Comment on the morphology of the red blood cells.
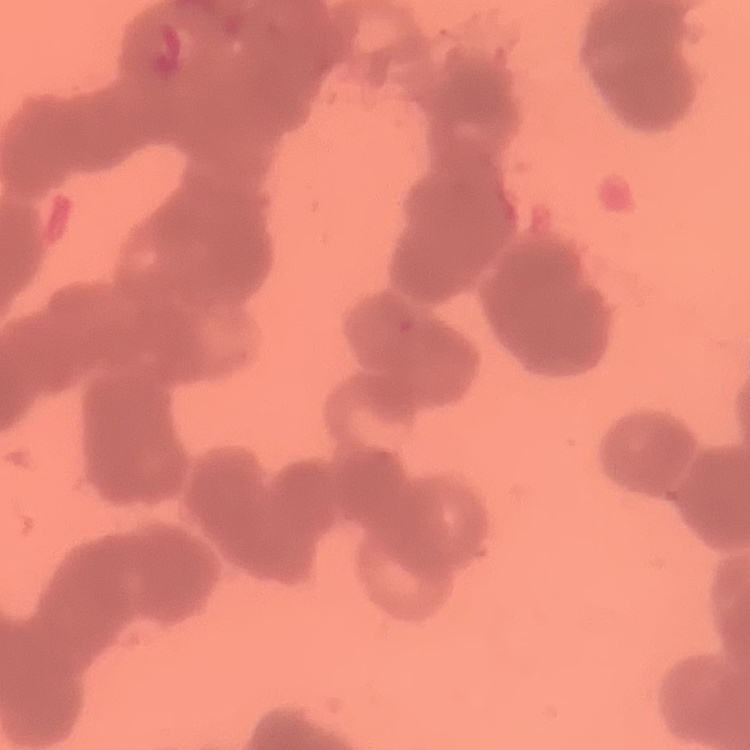

They show rouleaux formation.

Summary:
  - Preparation: thin blood film
  - Stain: Field's or Giemsa
  - Image type: square crop of a larger photomicrograph